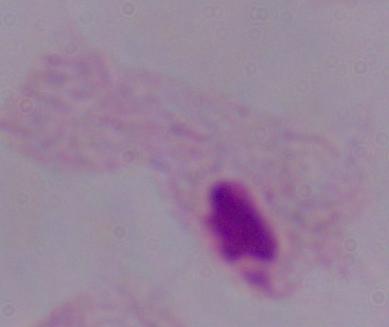

Summary:
  - Modality: micrograph
  - Magnification: 1000x
  - Identification: trichomonad